Assess this cell for malaria.
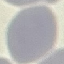

Uninfected.

stain = Giemsa
image type = cell patch, automatically extracted from a larger field of view and resized to 64 × 64 pixels
capture = smartphone through the microscope eyepiece
preparation = thin smear